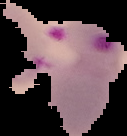

Segmented cell region on a black background. Image is 127×136 pixels. From a thin blood smear. Malaria status: parasitized.